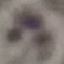

Summary:
  - Malaria status: uninfected
  - Preparation: thin blood film
  - Image type: automatically extracted cell patch, resized to 64 × 64 pixels
  - Capture: smartphone through the microscope eyepiece
  - Stain: Giemsa